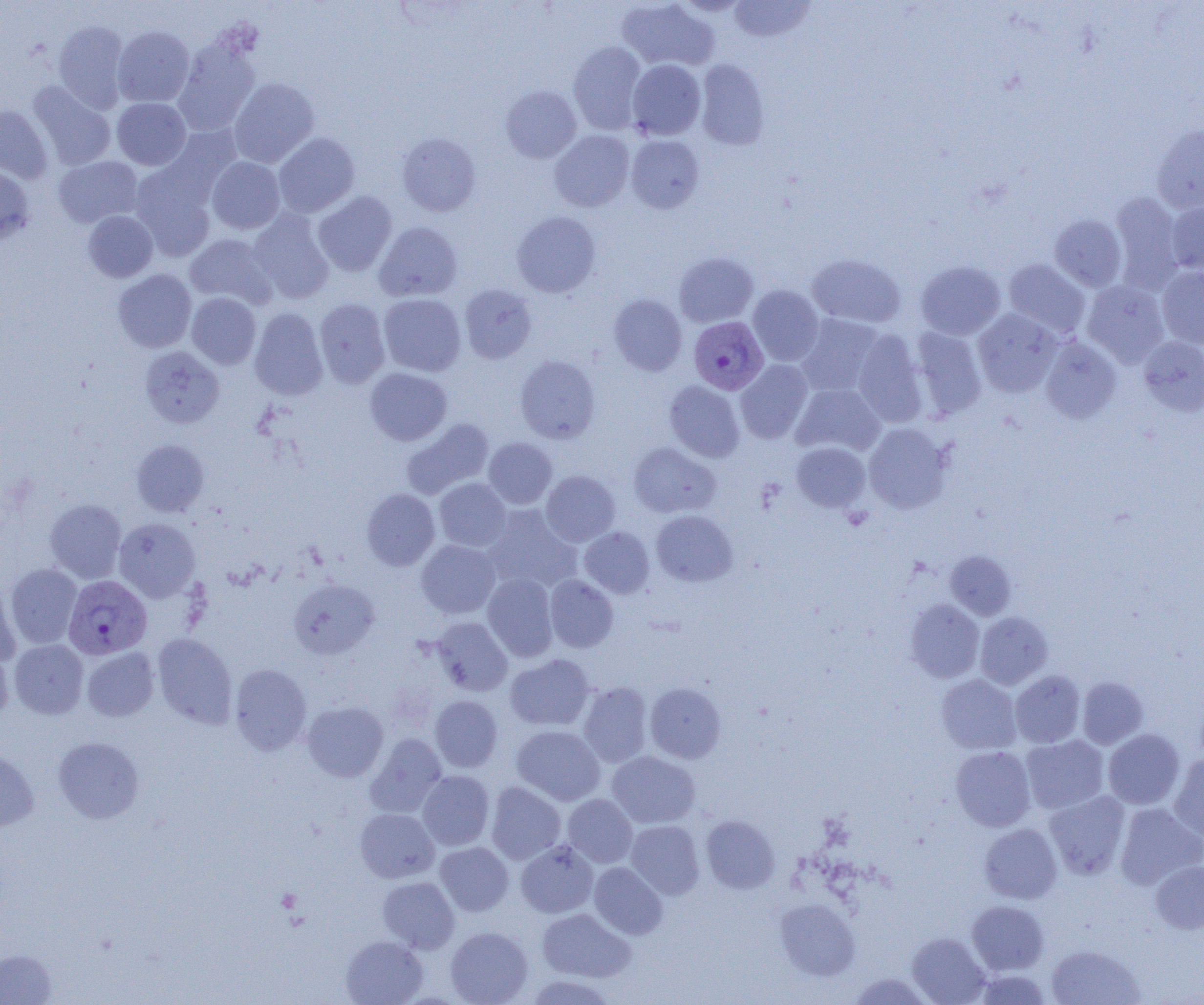 Approximate bounding boxes as named x1/y1/x2/y2 corners in pixels. Plasmodium vivax-infected red blood cell locations: (x1=689, y1=316, x2=768, y2=394), (x1=63, y1=575, x2=152, y2=660). Uninfected red blood cell locations: (x1=617, y1=0, x2=719, y2=71), (x1=729, y1=0, x2=815, y2=42), (x1=54, y1=21, x2=129, y2=112), (x1=113, y1=26, x2=194, y2=107), (x1=174, y1=39, x2=260, y2=135), (x1=568, y1=41, x2=648, y2=134), (x1=627, y1=59, x2=706, y2=140), (x1=695, y1=60, x2=770, y2=150), (x1=228, y1=78, x2=319, y2=167), (x1=28, y1=81, x2=116, y2=171), (x1=501, y1=85, x2=582, y2=163), (x1=112, y1=98, x2=190, y2=170), (x1=0, y1=105, x2=52, y2=183), (x1=158, y1=123, x2=242, y2=204), (x1=1152, y1=124, x2=1204, y2=214), (x1=550, y1=130, x2=634, y2=212), (x1=273, y1=133, x2=360, y2=217), (x1=397, y1=133, x2=481, y2=216), (x1=626, y1=135, x2=705, y2=213), (x1=54, y1=156, x2=142, y2=228), (x1=207, y1=157, x2=285, y2=234), (x1=0, y1=165, x2=35, y2=243), (x1=130, y1=165, x2=217, y2=261), (x1=312, y1=191, x2=397, y2=276), (x1=1110, y1=192, x2=1185, y2=292), (x1=1166, y1=201, x2=1204, y2=274), (x1=248, y1=209, x2=333, y2=303), (x1=83, y1=210, x2=158, y2=282), (x1=512, y1=211, x2=601, y2=297), (x1=1049, y1=214, x2=1127, y2=291), (x1=374, y1=222, x2=462, y2=302), (x1=184, y1=233, x2=277, y2=309), (x1=674, y1=252, x2=758, y2=327), (x1=807, y1=253, x2=906, y2=328), (x1=1003, y1=259, x2=1090, y2=338), (x1=916, y1=261, x2=1005, y2=339), (x1=1157, y1=266, x2=1204, y2=349), (x1=113, y1=269, x2=197, y2=352), (x1=1082, y1=281, x2=1169, y2=367), (x1=459, y1=284, x2=537, y2=363), (x1=748, y1=285, x2=824, y2=365), (x1=187, y1=292, x2=261, y2=369), (x1=379, y1=294, x2=466, y2=377), (x1=609, y1=294, x2=687, y2=376), (x1=314, y1=298, x2=390, y2=388), (x1=249, y1=308, x2=328, y2=400), (x1=973, y1=309, x2=1062, y2=397), (x1=796, y1=314, x2=885, y2=398), (x1=910, y1=327, x2=987, y2=419), (x1=851, y1=329, x2=927, y2=426), (x1=1040, y1=336, x2=1121, y2=423), (x1=1139, y1=336, x2=1204, y2=416), (x1=140, y1=346, x2=224, y2=427), (x1=515, y1=355, x2=600, y2=443), (x1=735, y1=359, x2=813, y2=443), (x1=365, y1=367, x2=452, y2=445), (x1=664, y1=380, x2=745, y2=462), (x1=791, y1=384, x2=885, y2=457), (x1=402, y1=418, x2=494, y2=499), (x1=863, y1=423, x2=953, y2=513), (x1=483, y1=437, x2=557, y2=509), (x1=131, y1=439, x2=210, y2=517), (x1=791, y1=441, x2=871, y2=513), (x1=628, y1=442, x2=720, y2=518), (x1=541, y1=471, x2=620, y2=546), (x1=434, y1=478, x2=511, y2=551), (x1=361, y1=488, x2=440, y2=571), (x1=45, y1=499, x2=127, y2=583), (x1=482, y1=505, x2=580, y2=592), (x1=651, y1=510, x2=738, y2=587), (x1=114, y1=517, x2=201, y2=602), (x1=579, y1=526, x2=654, y2=597), (x1=416, y1=540, x2=500, y2=618), (x1=945, y1=550, x2=1016, y2=620), (x1=5, y1=563, x2=82, y2=648), (x1=483, y1=574, x2=558, y2=661), (x1=545, y1=575, x2=618, y2=652), (x1=0, y1=576, x2=21, y2=667), (x1=288, y1=578, x2=380, y2=659), (x1=905, y1=599, x2=984, y2=682), (x1=975, y1=612, x2=1053, y2=689), (x1=430, y1=617, x2=512, y2=695), (x1=153, y1=633, x2=237, y2=729), (x1=9, y1=639, x2=88, y2=718), (x1=0, y1=644, x2=13, y2=724), (x1=82, y1=647, x2=158, y2=721), (x1=505, y1=654, x2=594, y2=731), (x1=230, y1=663, x2=311, y2=755), (x1=1010, y1=670, x2=1085, y2=748), (x1=937, y1=674, x2=1021, y2=754), (x1=1077, y1=676, x2=1148, y2=749), (x1=578, y1=682, x2=652, y2=767), (x1=645, y1=682, x2=726, y2=763), (x1=430, y1=695, x2=502, y2=772), (x1=302, y1=701, x2=388, y2=782), (x1=511, y1=725, x2=605, y2=805), (x1=1103, y1=729, x2=1184, y2=809), (x1=365, y1=734, x2=447, y2=817), (x1=1021, y1=735, x2=1109, y2=814), (x1=53, y1=737, x2=144, y2=823), (x1=0, y1=745, x2=39, y2=832), (x1=950, y1=746, x2=1035, y2=831), (x1=607, y1=751, x2=700, y2=828), (x1=1169, y1=754, x2=1204, y2=845), (x1=417, y1=770, x2=494, y2=850), (x1=485, y1=782, x2=566, y2=864), (x1=1044, y1=790, x2=1130, y2=879), (x1=563, y1=794, x2=637, y2=867), (x1=1115, y1=803, x2=1204, y2=889), (x1=356, y1=808, x2=439, y2=882), (x1=701, y1=815, x2=779, y2=893), (x1=626, y1=820, x2=705, y2=899), (x1=979, y1=823, x2=1062, y2=903), (x1=516, y1=841, x2=598, y2=917), (x1=435, y1=842, x2=513, y2=916), (x1=1151, y1=860, x2=1204, y2=934), (x1=589, y1=862, x2=668, y2=939), (x1=377, y1=876, x2=459, y2=953), (x1=776, y1=898, x2=860, y2=980), (x1=967, y1=901, x2=1049, y2=974), (x1=537, y1=908, x2=635, y2=982), (x1=446, y1=926, x2=532, y2=1005), (x1=907, y1=933, x2=990, y2=1004), (x1=341, y1=935, x2=428, y2=1005), (x1=1046, y1=944, x2=1145, y2=1005), (x1=0, y1=949, x2=57, y2=1005), (x1=976, y1=969, x2=1051, y2=1004), (x1=850, y1=972, x2=931, y2=1005), (x1=524, y1=974, x2=616, y2=1004). Slide-level diagnosis: Plasmodium vivax. Optical microscopy. 1000x magnification. Single field of view. Thin blood film. Image is 1204×1005 pixels.